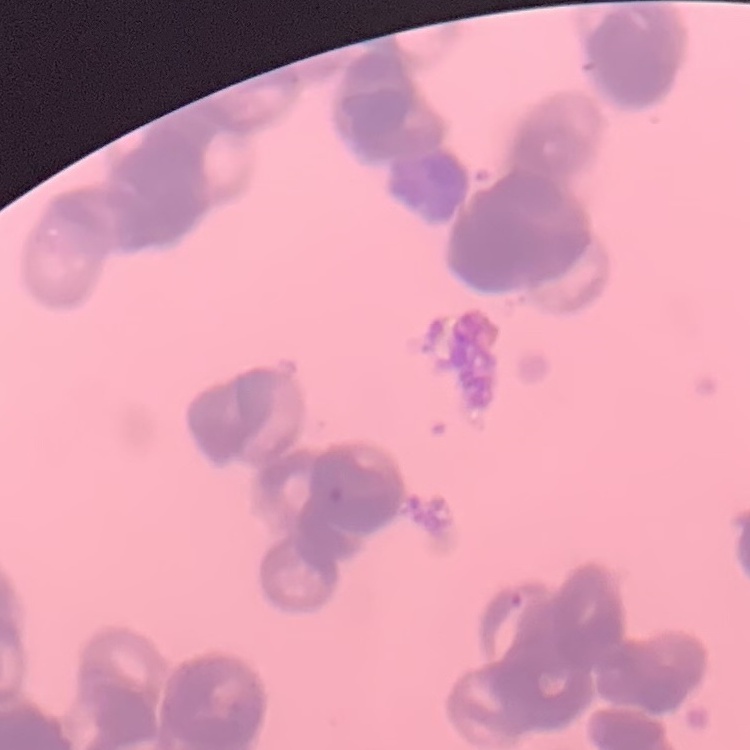

Summary:
  - Erythrocyte morphology: rouleaux formation
  - Stain: Field's or Giemsa
  - Image type: square crop of a larger photomicrograph
  - Preparation: thin peripheral smear